Name the cell type shown.
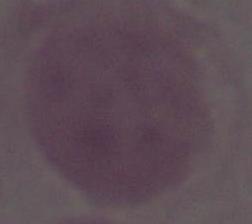

An erythrocyte.

Captured at 1000x magnification. Photomicrograph.